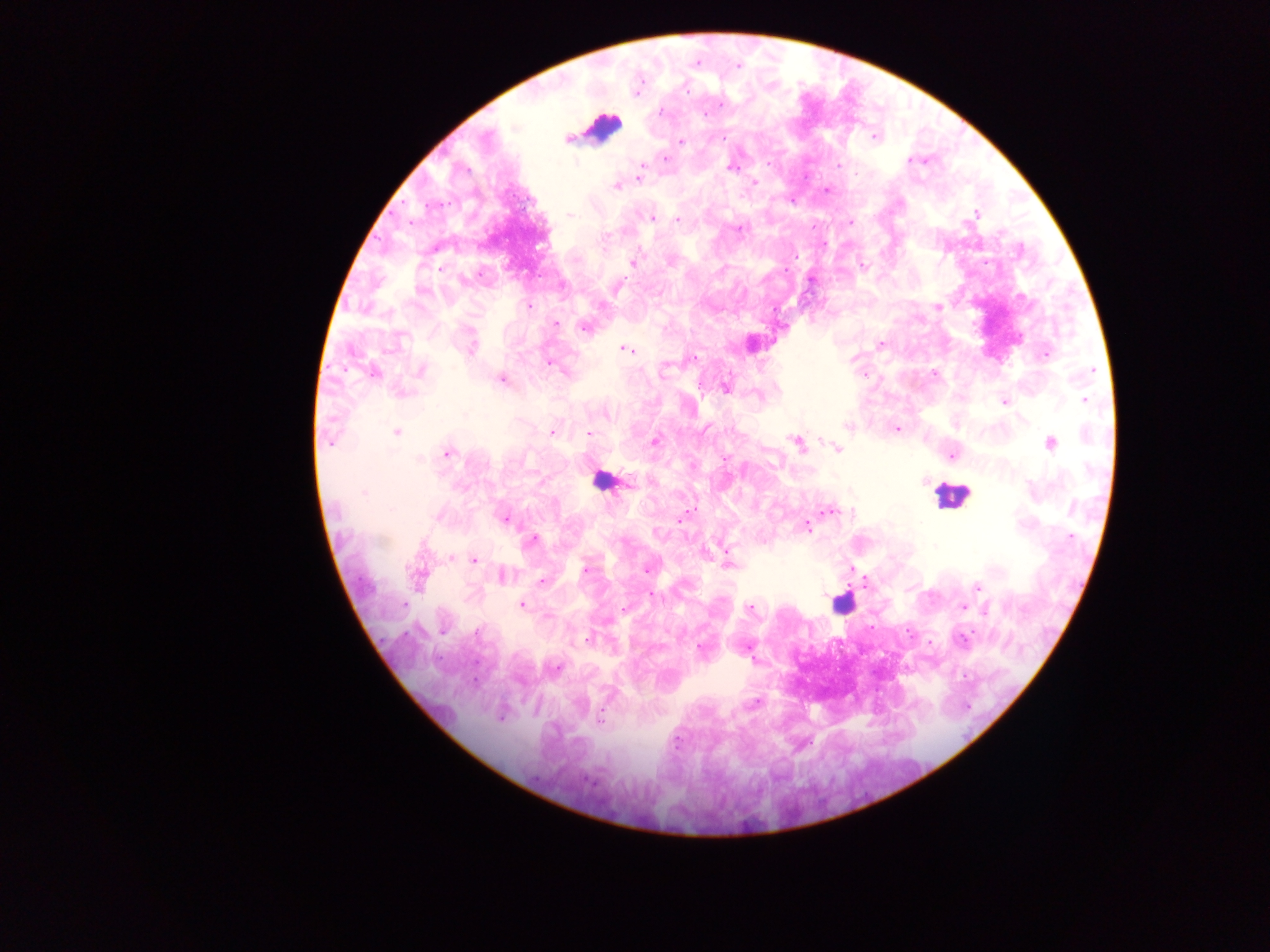 Approximate centers as x y in pixels. Leukocyte locations: 603 125; 601 479; 952 496; 841 603. Plasmodium parasite locations: 738 66; 721 104; 661 111; 704 114; 874 137; 723 138; 567 140; 681 141; 665 158; 910 159; 768 162; 576 163; 640 168; 731 168; 639 177; 754 183; 616 187; 828 191; 791 201; 571 214; 975 214; 652 219; 677 220; 851 223; 740 229; 605 236; 633 262; 670 262; 441 268; 529 307; 937 307; 556 324; 585 327; 880 344; 471 347; 625 349; 1046 355; 692 358; 550 363; 665 367; 421 370; 1092 371; 564 372; 374 373; 935 374; 864 375; 502 380; 726 388; 401 394; 1085 400; 1005 402; 607 416; 848 427; 897 429; 551 432; 396 433; 588 434; 655 441; 330 442; 796 443; 1050 444; 837 449; 447 452; 951 456; 419 459; 628 483; 364 492; 831 511; 438 516; 682 518; 505 519; 808 526; 1070 537; 532 539; 935 546; 451 558; 475 561; 728 565; 586 570; 646 570; 418 575; 503 577; 541 581; 978 587; 651 595; 404 605; 522 605; 964 607; 750 608; 623 609; 985 611; 443 631; 476 633; 588 639; 962 639; 699 649; 556 667; 501 717; 600 717; 677 744. Single field of view. Sample from Ghana. Image is 1270×952 pixels. Mobile-phone photograph taken through the microscope. Thick blood film.